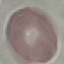 Malaria status: uninfected. Thin smear of blood. Acquired by smartphone through the microscope eyepiece. Giemsa-stained preparation. Cell patch, automatically extracted from a larger field of view and resized to 64 × 64 pixels.